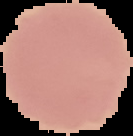

From a thin blood smear. Result: negative for Plasmodium parasites. Cell region segmented out of the field of view; the surrounding area is masked to black. Image is 133×136 pixels.